Give the extent of all uninfected red blood cells.
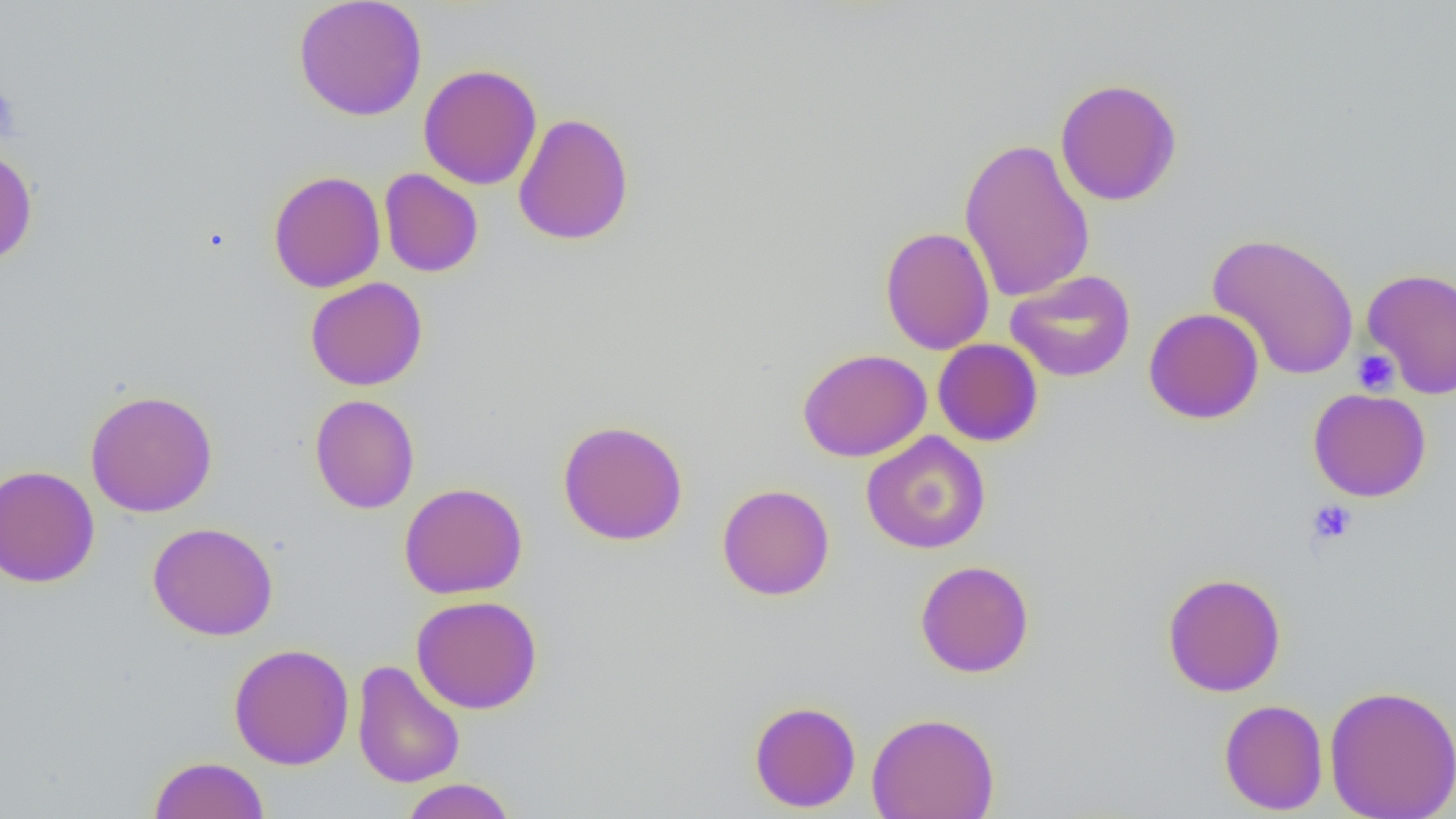
Approximate bounding boxes as named x1/y1/x2/y2 corners in pixels.
Uninfected red blood cells: (x1=292, y1=0, x2=428, y2=121), (x1=418, y1=64, x2=543, y2=190), (x1=1054, y1=77, x2=1183, y2=206), (x1=513, y1=112, x2=634, y2=246), (x1=958, y1=137, x2=1095, y2=304), (x1=0, y1=146, x2=38, y2=266), (x1=379, y1=168, x2=483, y2=278), (x1=267, y1=170, x2=386, y2=292), (x1=880, y1=226, x2=995, y2=355), (x1=1207, y1=231, x2=1360, y2=381), (x1=1361, y1=267, x2=1456, y2=399), (x1=1005, y1=269, x2=1136, y2=383), (x1=305, y1=277, x2=428, y2=391), (x1=1143, y1=307, x2=1264, y2=424), (x1=932, y1=338, x2=1043, y2=447), (x1=797, y1=348, x2=932, y2=463), (x1=1307, y1=388, x2=1432, y2=502), (x1=84, y1=389, x2=219, y2=518), (x1=309, y1=394, x2=420, y2=514), (x1=557, y1=419, x2=689, y2=546), (x1=860, y1=431, x2=992, y2=554), (x1=0, y1=465, x2=100, y2=588), (x1=399, y1=482, x2=528, y2=599), (x1=717, y1=483, x2=835, y2=601), (x1=148, y1=522, x2=279, y2=641), (x1=915, y1=560, x2=1034, y2=678), (x1=1162, y1=572, x2=1286, y2=697), (x1=410, y1=595, x2=543, y2=714), (x1=228, y1=643, x2=354, y2=770), (x1=351, y1=659, x2=465, y2=789), (x1=1324, y1=684, x2=1456, y2=819), (x1=1219, y1=698, x2=1328, y2=815), (x1=748, y1=700, x2=861, y2=812), (x1=866, y1=711, x2=1000, y2=819), (x1=148, y1=755, x2=270, y2=819), (x1=399, y1=778, x2=516, y2=818).

slide_level_diagnosis: negative for blood parasites
platelet_locations: 'approximate bounding boxes as named x1/y1/x2/y2 corners in pixels: (x1=0, y1=85, x2=21, y2=143), (x1=1352, y1=349, x2=1400, y2=395), (x1=1307, y1=499, x2=1357, y2=545)'
image_size: 1456×819 pixels
modality: light microscopy
field_of_view: single
preparation: thin blood film
magnification: 1000x